Assess this cell for malaria.
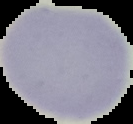

It is uninfected.

Segmented cell region on a black background. Image is 133×124 pixels. From a thin blood film.